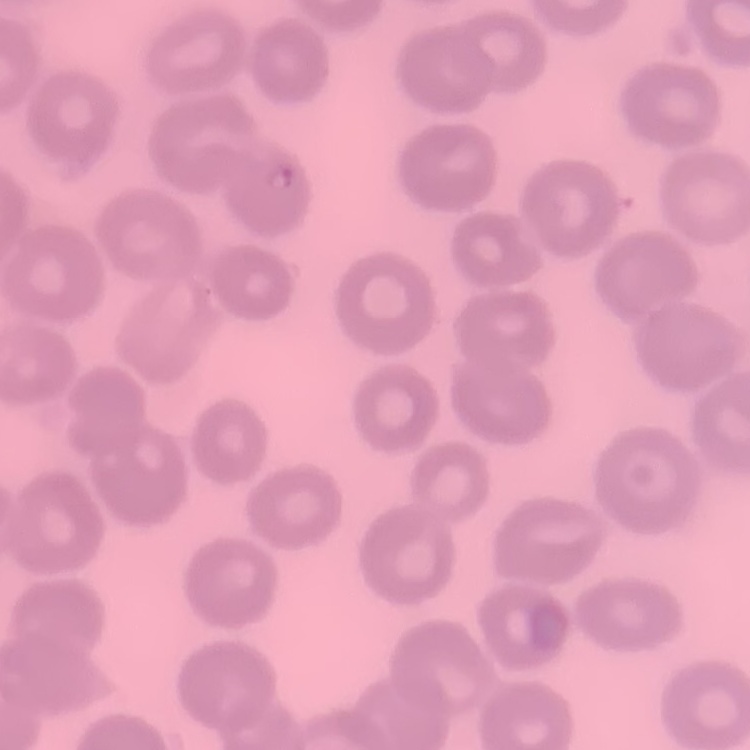

erythrocyte morphology = no rouleaux formation
image type = one tile cut from a larger photomicrograph
preparation = thin blood film
stain = Field's or Giemsa